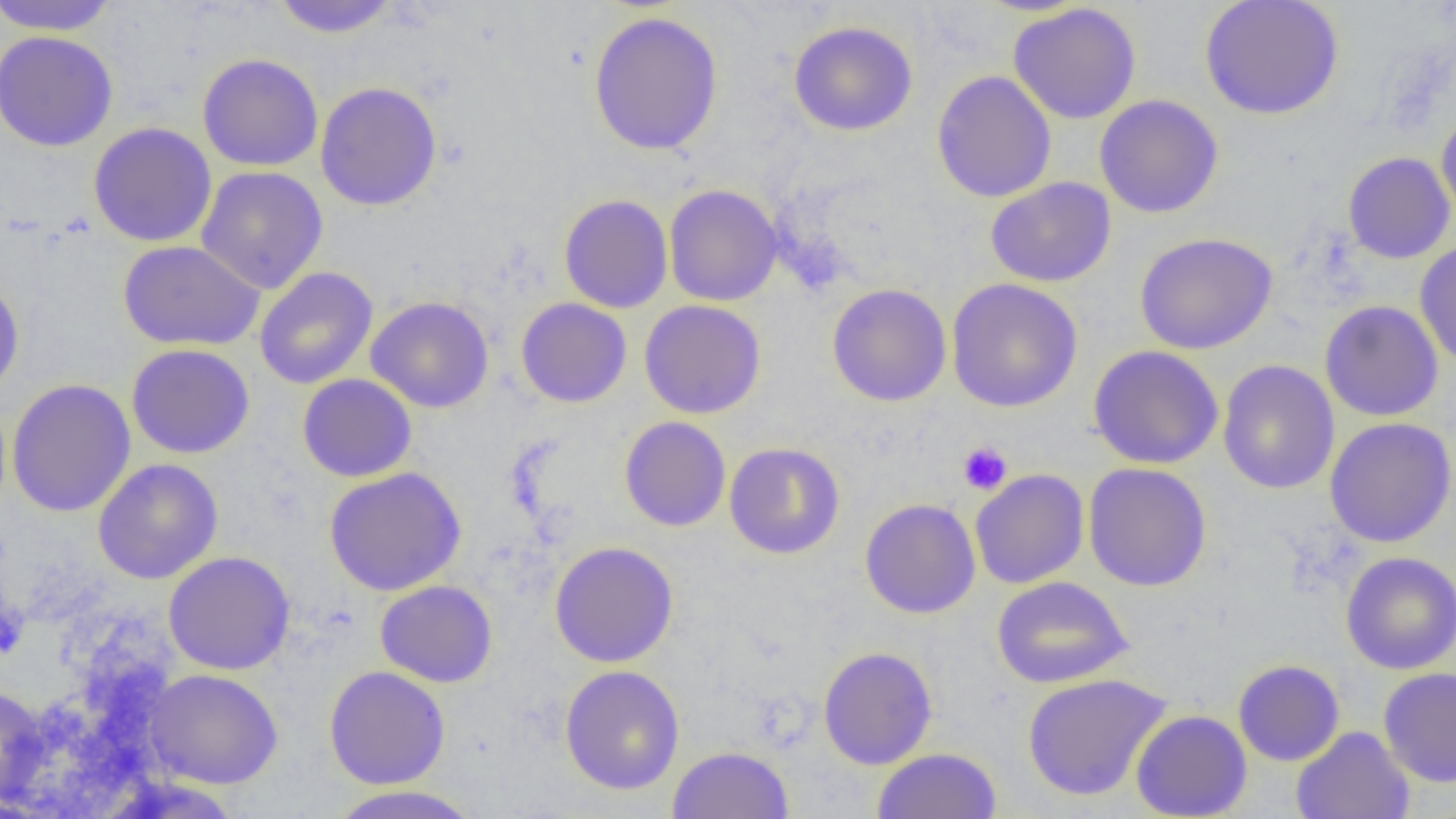
slide-level diagnosis = no evidence of blood parasites
uninfected red blood cell locations = approximate bounding boxes as (x1, y1, x2, y2) in pixels: (0, 0, 119, 36), (271, 0, 399, 38), (1200, 0, 1344, 120), (1008, 3, 1142, 124), (588, 11, 724, 155), (788, 20, 918, 136), (0, 30, 118, 152), (197, 53, 324, 171), (932, 70, 1057, 203), (315, 81, 442, 211), (1094, 94, 1224, 218), (1436, 104, 1456, 223), (88, 122, 217, 247), (1342, 151, 1455, 264), (196, 165, 328, 294), (985, 177, 1116, 287), (664, 184, 783, 307), (559, 194, 673, 313), (1135, 232, 1277, 354), (1415, 239, 1456, 369), (118, 240, 265, 350), (254, 267, 378, 390), (0, 274, 25, 400), (946, 278, 1083, 413), (827, 283, 952, 407), (366, 296, 494, 413), (516, 297, 632, 408), (639, 299, 766, 419), (1320, 300, 1443, 421), (127, 343, 255, 459), (1088, 345, 1224, 470), (1217, 360, 1340, 495), (297, 374, 417, 482), (6, 379, 137, 518), (619, 416, 731, 532), (1325, 416, 1456, 548), (724, 442, 845, 559), (93, 458, 223, 584), (1083, 462, 1212, 592), (323, 467, 467, 596), (970, 469, 1089, 589), (859, 498, 981, 619), (549, 541, 679, 668), (163, 551, 295, 675), (1340, 551, 1456, 674), (991, 576, 1133, 688), (375, 580, 497, 688), (818, 646, 938, 770), (1233, 659, 1345, 766), (559, 665, 685, 795), (323, 666, 451, 789), (1378, 666, 1456, 788), (143, 669, 284, 789), (1022, 673, 1171, 802), (0, 684, 50, 808), (1131, 709, 1252, 818), (1291, 726, 1415, 819), (667, 745, 794, 818), (871, 747, 1001, 818), (326, 785, 483, 819)
preparation = thin blood smear
platelet locations = approximate bounding boxes as (x1, y1, x2, y2) in pixels: (957, 441, 1013, 495), (0, 602, 28, 659)
image size = 1456×819 pixels
modality = optical microscopy
field of view = one of a larger specimen
magnification = 1000x